State which cell type is depicted.
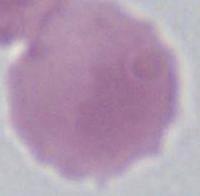

An erythrocyte.

modality: micrograph
magnification: 1000x